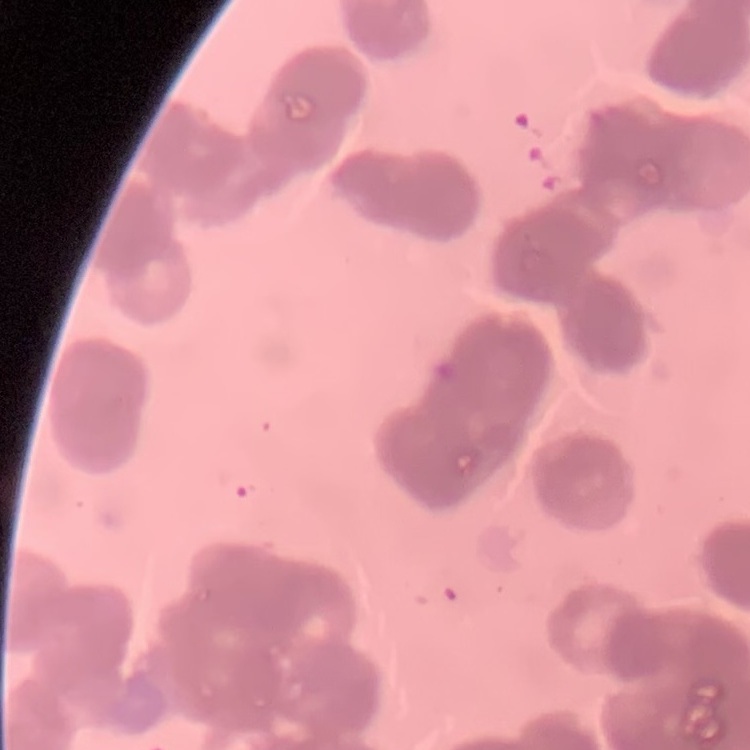

Summary:
  - Erythrocyte morphology: rouleaux formation
  - Image type: one tile cut from a larger photomicrograph
  - Stain: Field's or Giemsa
  - Preparation: thin peripheral smear